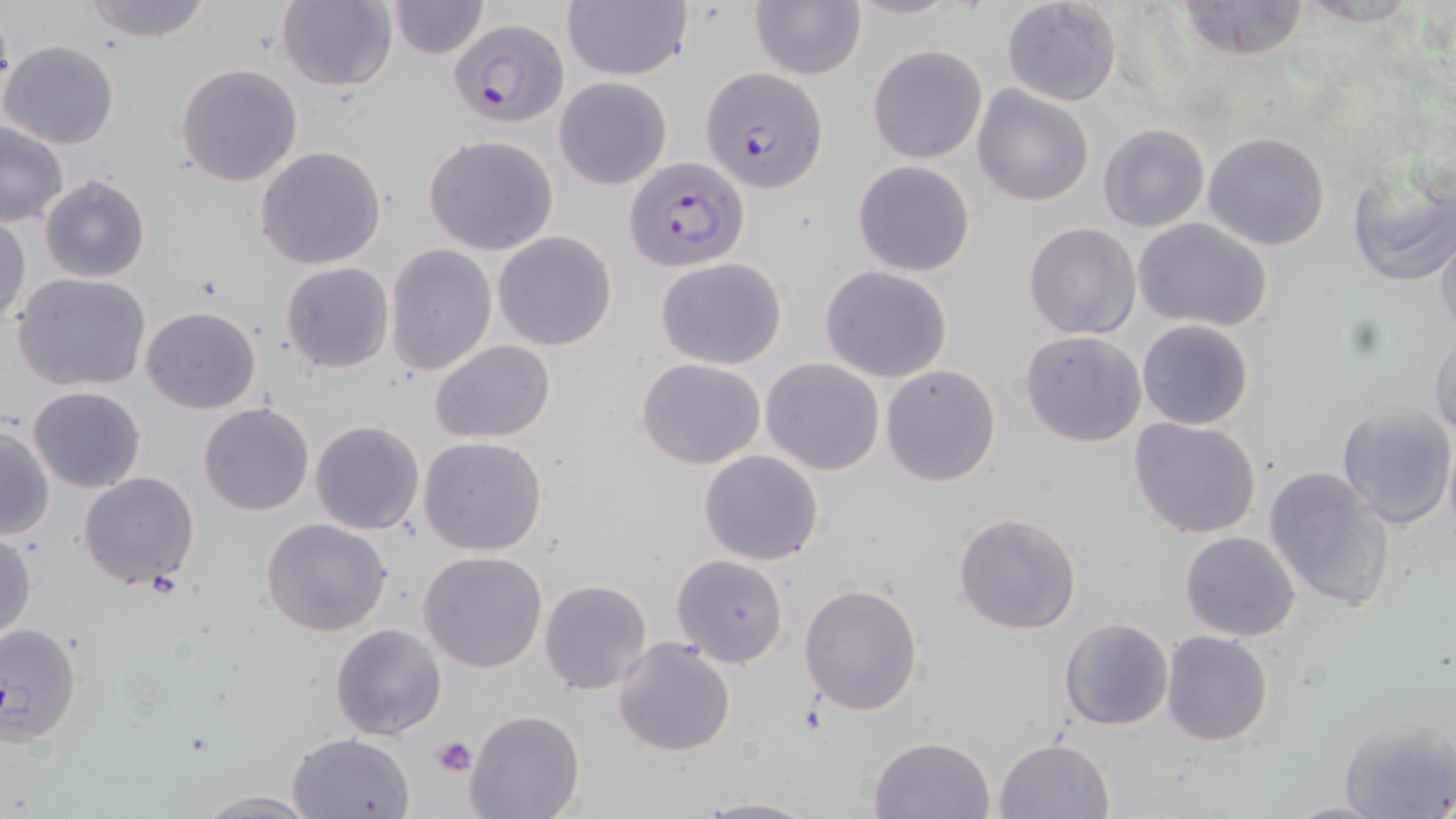

Approximate bounding boxes as (x1,y1)-(x2,y2) corner pairs in pixels. Platelet locations: (431,735)-(477,778). Uninfected red blood cell locations: (79,0)-(215,42), (387,0)-(489,59), (844,0)-(964,21), (1000,0)-(1124,107), (1176,0)-(1312,63), (275,1)-(397,91), (559,1)-(692,82), (751,2)-(865,80), (2,38)-(120,149), (866,44)-(988,164), (176,63)-(304,188), (553,76)-(673,190), (974,87)-(1092,206), (0,123)-(69,226), (1098,123)-(1210,232), (1203,131)-(1330,250), (423,134)-(558,255), (255,145)-(387,269), (853,159)-(975,277), (1345,161)-(1456,289), (39,174)-(150,283), (0,215)-(29,327), (1135,218)-(1275,333), (1024,222)-(1142,340), (1433,224)-(1456,338), (492,231)-(617,351), (386,244)-(496,376), (655,256)-(788,370), (279,262)-(395,372), (819,266)-(952,384), (12,273)-(153,391), (141,306)-(263,415), (1137,319)-(1255,431), (1020,330)-(1147,446), (1428,331)-(1456,442), (431,340)-(555,445), (760,357)-(886,475), (637,358)-(766,470), (881,363)-(1001,486), (27,385)-(146,494), (1336,402)-(1456,530), (197,403)-(315,517), (1129,417)-(1261,538), (310,420)-(424,535), (0,424)-(55,541), (418,436)-(548,555), (699,449)-(822,566), (1264,466)-(1396,613), (79,471)-(200,590), (952,512)-(1082,635), (261,518)-(393,637), (0,530)-(37,643), (1180,531)-(1301,641), (418,552)-(548,674), (671,554)-(788,668), (539,578)-(652,696), (798,584)-(924,716), (1059,617)-(1173,731), (0,620)-(83,744), (330,623)-(447,741), (1161,631)-(1273,746), (611,637)-(737,757), (464,710)-(585,819), (1338,716)-(1454,818), (286,732)-(415,818), (867,735)-(995,818), (993,736)-(1115,819), (190,789)-(321,819), (692,795)-(819,818), (1282,798)-(1390,818). Plasmodium falciparum-infected red blood cell locations: (446,18)-(565,126), (701,66)-(829,194), (625,156)-(749,271). Slide-level diagnosis: Plasmodium falciparum. Captured at 1000x magnification. Optical microscopy. Thin blood film. May-Grünwald-Giemsa-stained preparation. One field of a larger specimen. Image is 1456×819 pixels.